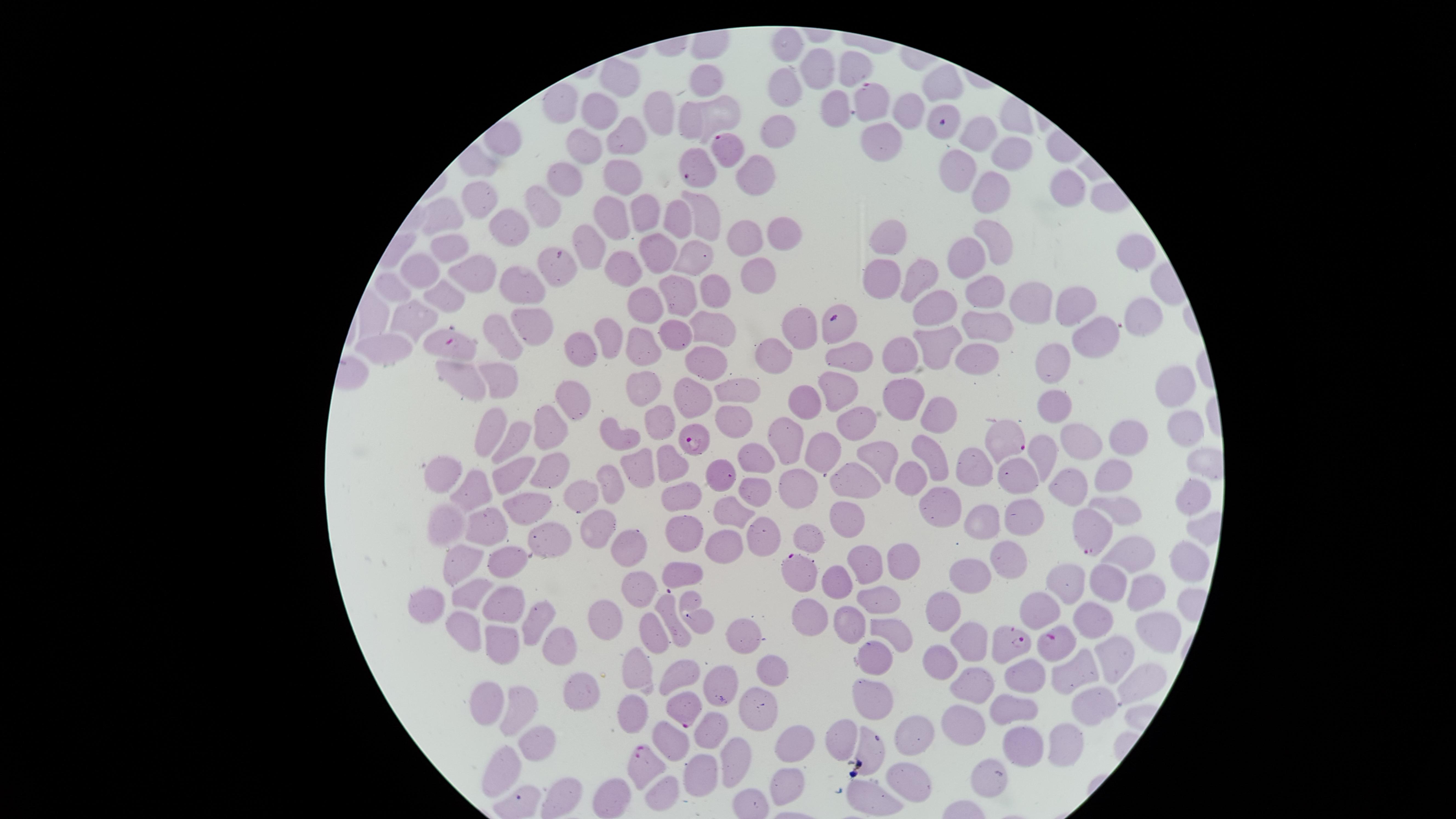 Approximate marker points as {x, y} in pixels. Uninfected red blood cells: {788, 49}, {819, 65}, {853, 66}, {706, 77}, {944, 80}, {623, 82}, {782, 85}, {556, 103}, {837, 105}, {597, 111}, {660, 111}, {911, 112}, {722, 114}, {692, 122}, {629, 130}, {777, 130}, {975, 134}, {885, 141}, {578, 145}, {1007, 149}, {962, 167}, {758, 174}, {631, 176}, {564, 177}, {1064, 187}, {991, 190}, {479, 200}, {540, 203}, {646, 214}, {699, 216}, {447, 218}, {613, 218}, {672, 218}, {506, 219}, {779, 234}, {744, 235}, {886, 235}, {589, 241}, {1000, 243}, {449, 250}, {696, 250}, {1135, 252}, {973, 253}, {655, 266}, {423, 267}, {474, 267}, {624, 272}, {757, 272}, {885, 272}, {926, 278}, {518, 287}, {714, 288}, {986, 291}, {669, 294}, {446, 295}, {394, 298}, {1070, 300}, {1022, 302}, {932, 307}, {647, 310}, {1142, 313}, {530, 318}, {410, 323}, {994, 326}, {801, 331}, {676, 333}, {710, 333}, {500, 334}, {1097, 335}, {612, 340}, {585, 342}, {939, 343}, {635, 350}, {389, 353}, {902, 353}, {857, 356}, {972, 356}, {770, 360}, {1054, 360}, {704, 364}, {459, 369}, {498, 373}, {732, 387}, {646, 388}, {1176, 391}, {839, 392}, {897, 392}, {694, 393}, {809, 397}, {576, 401}, {1058, 401}, {934, 414}, {734, 418}, {495, 423}, {657, 427}, {550, 429}, {1184, 429}, {857, 430}, {516, 436}, {621, 439}, {1129, 439}, {791, 440}, {1092, 442}, {826, 447}, {1048, 451}, {760, 454}, {880, 456}, {931, 456}, {672, 459}, {636, 465}, {519, 470}, {556, 471}, {969, 471}, {1113, 473}, {1021, 474}, {855, 476}, {727, 478}, {449, 479}, {613, 481}, {1070, 482}, {795, 484}, {908, 484}, {579, 491}, {754, 494}, {473, 495}, {686, 495}, {1194, 500}, {1122, 503}, {945, 507}, {734, 510}, {1025, 514}, {533, 515}, {847, 515}, {983, 523}, {443, 525}, {594, 525}, {491, 531}, {811, 533}, {687, 536}, {759, 538}, {632, 541}, {553, 546}, {725, 549}, {1132, 553}, {1002, 554}, {460, 562}, {1185, 562}, {863, 563}, {908, 563}, {511, 564}, {969, 567}, {686, 571}, {636, 582}, {1068, 582}, {1115, 582}, {835, 586}, {1153, 589}, {471, 592}, {872, 603}, {939, 605}, {433, 607}, {509, 607}, {670, 609}, {697, 609}, {1046, 609}, {611, 612}, {1099, 615}, {807, 617}, {540, 618}, {465, 624}, {847, 626}, {1161, 626}, {658, 629}, {739, 629}, {889, 632}, {500, 641}, {969, 642}, {557, 644}, {939, 655}, {1111, 655}, {872, 660}, {1073, 667}, {765, 670}, {1034, 671}, {683, 672}, {640, 673}, {722, 678}, {1137, 678}, {977, 686}, {576, 693}, {1096, 694}, {873, 696}, {486, 704}, {637, 704}, {752, 704}, {1011, 708}, {519, 709}, {969, 716}, {709, 727}, {538, 733}, {911, 734}, {1071, 736}, {841, 737}, {676, 740}, {791, 745}, {870, 745}, {1021, 747}, {732, 760}, {498, 762}, {992, 765}, {697, 772}, {907, 773}, {782, 778}, {662, 791}, {871, 794}, {614, 797}. Parasitized red blood cells: {874, 101}, {940, 121}, {727, 148}, {693, 167}, {558, 262}, {838, 323}, {450, 343}, {700, 439}, {1006, 440}, {1085, 533}, {799, 572}, {1060, 640}, {1006, 643}, {683, 711}, {644, 763}. Smartphone photograph through the microscope eyepiece. Presence: malaria parasites detected. Species: Plasmodium falciparum. Giemsa stain. Thin blood film. One field of view of the specimen. Circular visible region. Image is 1456×819 pixels.